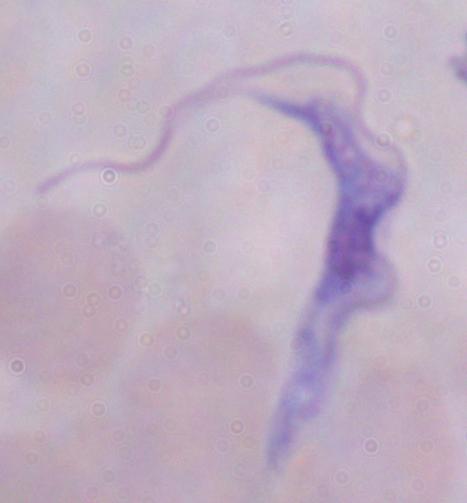

1000x magnification. Micrograph. A trypanosome is shown.